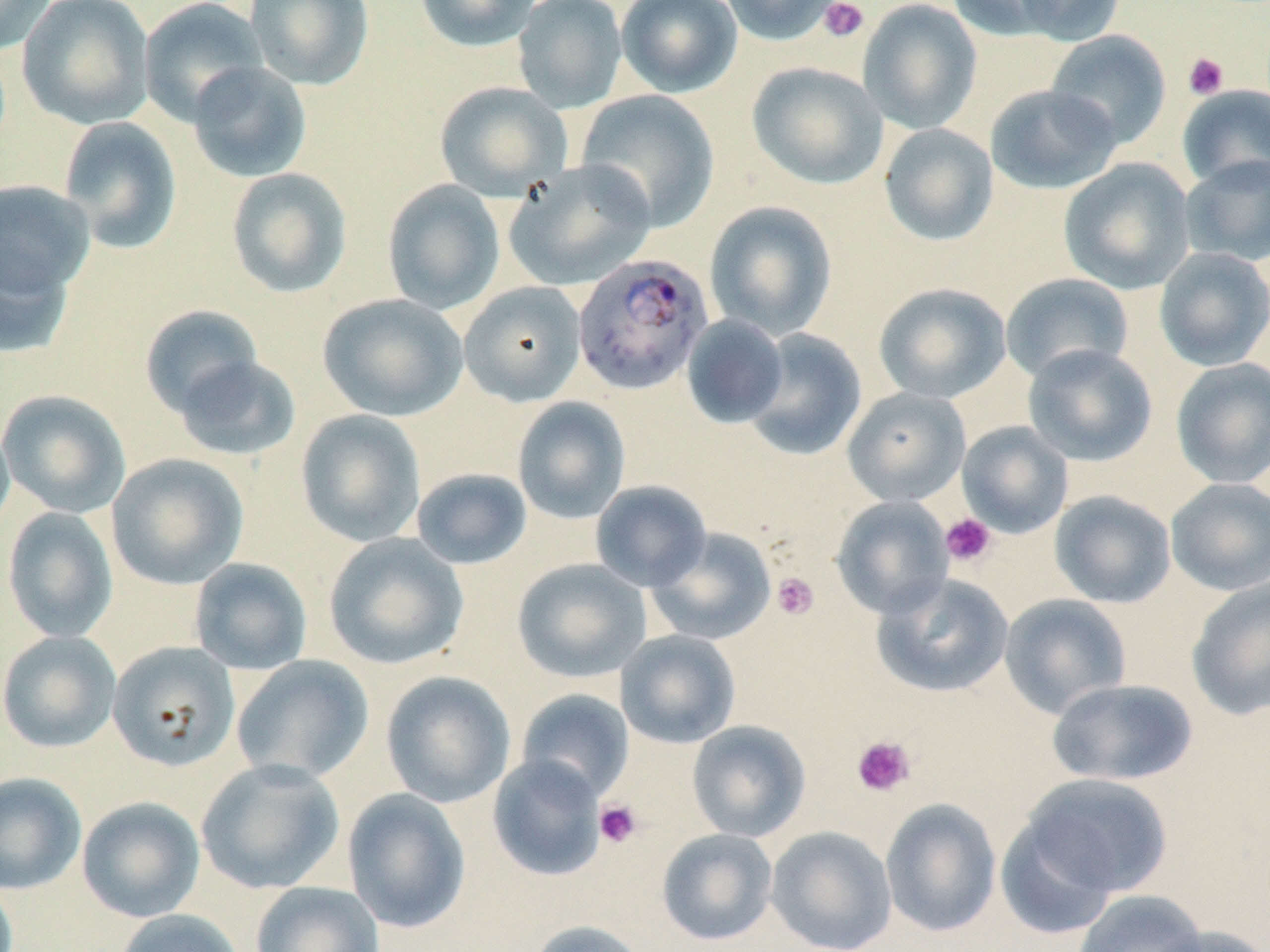
Summary:
  - Coordinate format: approximate bounding boxes as (x1, y1, x2, y2) in pixels
  - Plasmodium falciparum-infected red blood cell locations: (572, 252, 714, 395)
  - Uninfected red blood cell locations: (0, 0, 57, 55), (16, 0, 156, 130), (138, 0, 268, 127), (244, 0, 374, 90), (415, 0, 541, 53), (512, 0, 627, 113), (616, 0, 742, 98), (719, 0, 846, 47), (858, 0, 982, 134), (946, 0, 1069, 40), (1011, 0, 1127, 45), (1045, 29, 1172, 149), (187, 61, 313, 182), (747, 62, 888, 189), (434, 81, 572, 201), (985, 84, 1122, 194), (1177, 84, 1269, 190), (576, 89, 720, 231), (58, 116, 183, 254), (879, 123, 999, 247), (1179, 155, 1270, 266), (1059, 158, 1195, 295), (505, 159, 655, 291), (226, 167, 353, 298), (0, 180, 95, 304), (382, 180, 505, 315), (704, 200, 837, 340), (0, 239, 76, 359), (1154, 247, 1270, 371), (1000, 273, 1134, 383), (458, 281, 586, 406), (873, 282, 1011, 404), (318, 294, 468, 421), (139, 305, 264, 418), (681, 315, 788, 428), (744, 328, 867, 460), (1022, 344, 1158, 466), (173, 355, 301, 461), (1170, 357, 1270, 489), (843, 387, 970, 507), (0, 390, 131, 518), (513, 396, 631, 524), (295, 409, 427, 547), (0, 419, 15, 537), (957, 422, 1073, 538), (106, 453, 249, 589), (411, 468, 533, 570), (1165, 478, 1270, 596), (590, 480, 712, 591), (1050, 490, 1176, 608), (831, 496, 953, 619), (2, 506, 119, 643), (646, 527, 777, 646), (324, 532, 469, 670), (189, 558, 313, 675), (511, 558, 651, 683), (872, 573, 1015, 698), (1186, 576, 1270, 721), (1000, 593, 1132, 719), (616, 630, 741, 749), (0, 631, 121, 753), (107, 640, 240, 771), (231, 655, 375, 785), (381, 671, 516, 808), (1046, 678, 1198, 786), (515, 689, 634, 802), (687, 720, 811, 842), (487, 755, 607, 881), (196, 759, 345, 894), (0, 772, 86, 894), (1020, 773, 1174, 898), (342, 788, 471, 933), (77, 796, 205, 923), (880, 798, 1002, 937), (995, 814, 1119, 941), (766, 826, 897, 952), (656, 828, 778, 945), (250, 881, 384, 952), (1074, 889, 1207, 952), (113, 908, 245, 952), (526, 920, 650, 952), (1151, 925, 1269, 952)
  - Platelet locations: (818, 0, 869, 43), (1183, 52, 1229, 100), (941, 513, 997, 568), (771, 572, 820, 621), (851, 735, 916, 797), (594, 800, 643, 848)
  - Slide-level diagnosis: Plasmodium falciparum
  - Modality: light microscopy
  - Field of view: single
  - Stain: May-Grünwald-Giemsa
  - Preparation: thin blood film
  - Image size: 1270×952 pixels
  - Magnification: 1000x